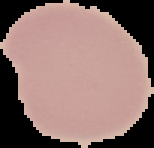
Segmented cell region on a black background. Result: negative for malaria parasites. Image is 154×148 pixels. From a thin blood smear.